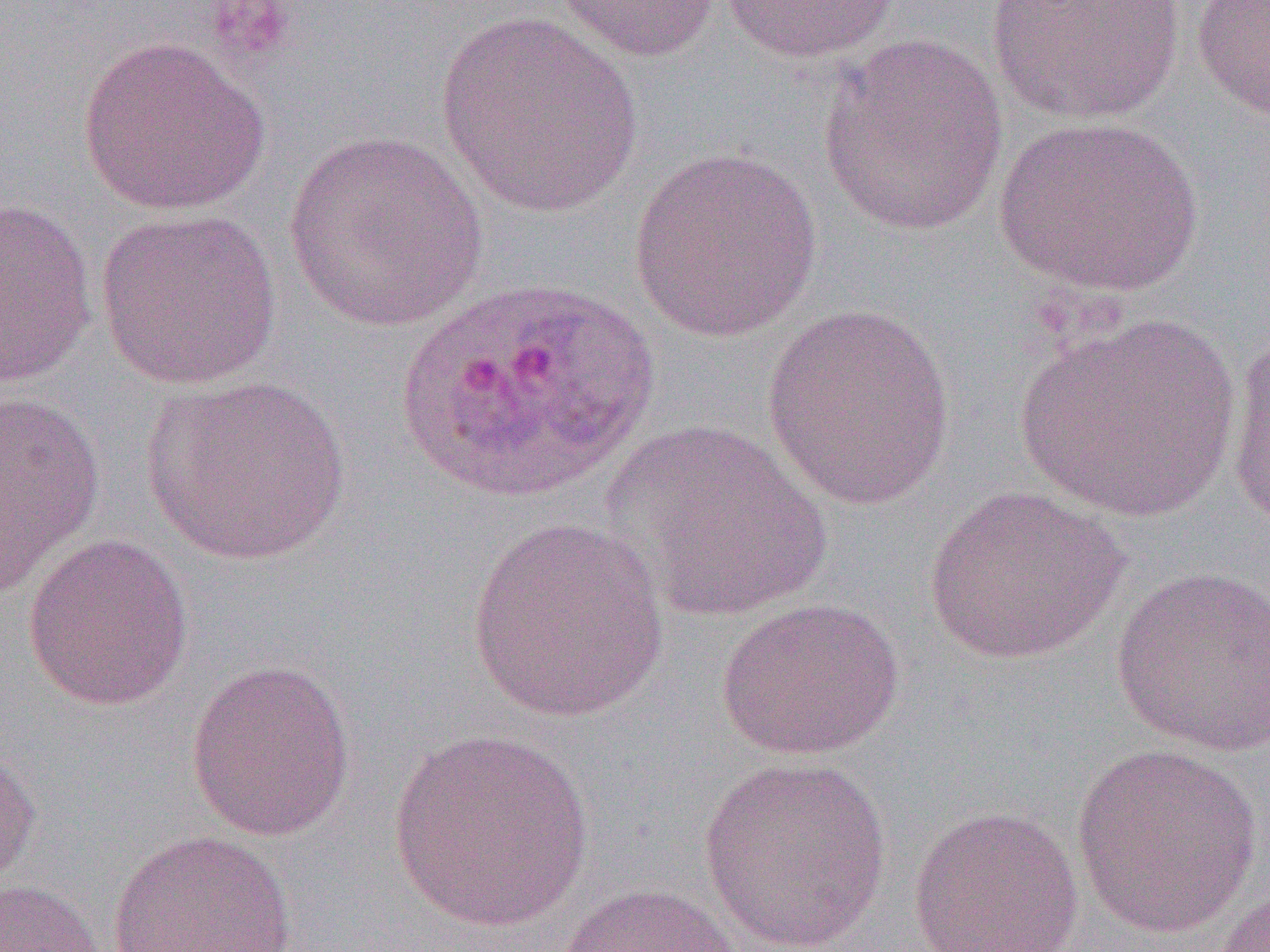
Summary:
  - Coordinate format: approximate bounding boxes as (x1,y1)-(x2,y2) corner pairs in pixels
  - Uninfected red blood cell locations: (552,0)-(722,63), (986,0)-(1186,125), (1190,0)-(1270,124), (719,1)-(901,64), (434,12)-(644,219), (818,35)-(1008,239), (77,37)-(271,216), (993,115)-(1206,297), (282,132)-(490,332), (627,147)-(822,343), (1,197)-(99,389), (93,208)-(284,390), (760,302)-(960,511), (1015,313)-(1241,525), (1225,322)-(1270,536), (139,375)-(352,567), (0,389)-(106,598), (602,418)-(831,622), (922,486)-(1131,665), (464,517)-(669,723), (22,533)-(194,711), (1110,565)-(1270,757), (715,597)-(906,762), (184,659)-(357,842), (387,730)-(595,933), (0,743)-(41,894), (1070,744)-(1264,939), (697,755)-(894,951), (907,805)-(1084,952), (107,829)-(297,952), (0,879)-(105,952), (553,882)-(750,952), (1211,887)-(1270,952)
  - Plasmodium ovale-infected red blood cell locations: (387,275)-(662,505)
  - Slide-level diagnosis: Plasmodium ovale
  - Magnification: 1000x
  - Image size: 1270×952 pixels
  - Preparation: thin blood film
  - Field of view: single
  - Modality: optical microscopy